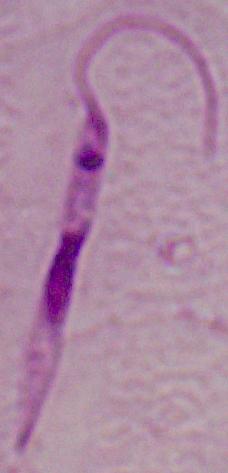
Micrograph. A Leishmania parasite is shown. Captured at 1000x magnification.